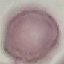
result = no malaria parasites seen
preparation = thin blood smear
capture = smartphone camera at the microscope eyepiece
image type = cell patch, automatically extracted from a larger field of view and resized to 64 × 64 pixels
stain = Giemsa